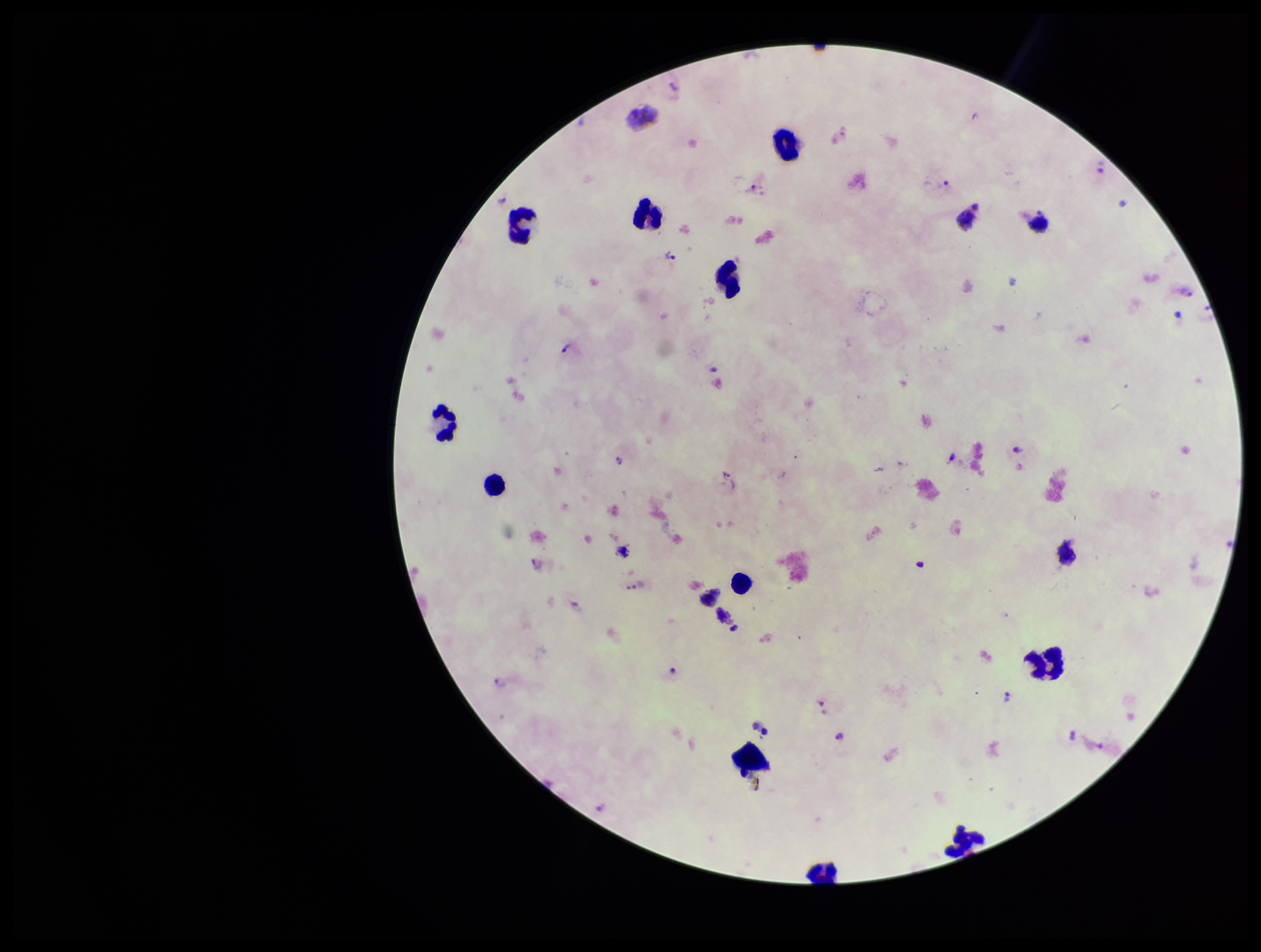
Species reported for this patient: Plasmodium vivax. Patient malaria status: infected. Single field of view. Plasmodium parasites: identified. Parasite count: 19. Photographed through the microscope eyepiece with a smartphone camera. Image is 1261×952 pixels. Stained with Giemsa. Leukocyte count: 12. Preparation: thick smear.